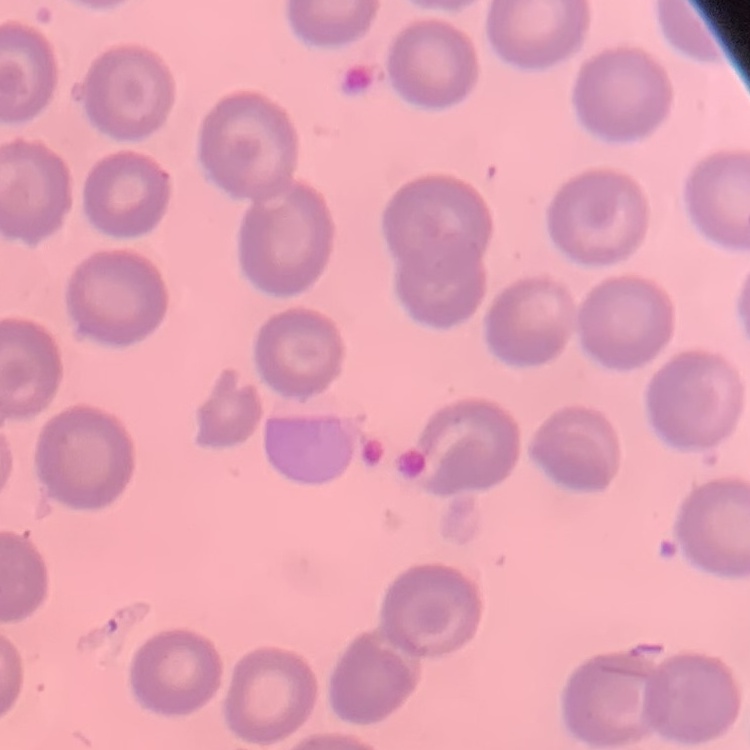
erythrocyte morphology = no rouleaux formation
preparation = thin blood smear
image type = one tile cut from a larger photomicrograph
stain = Field's or Giemsa